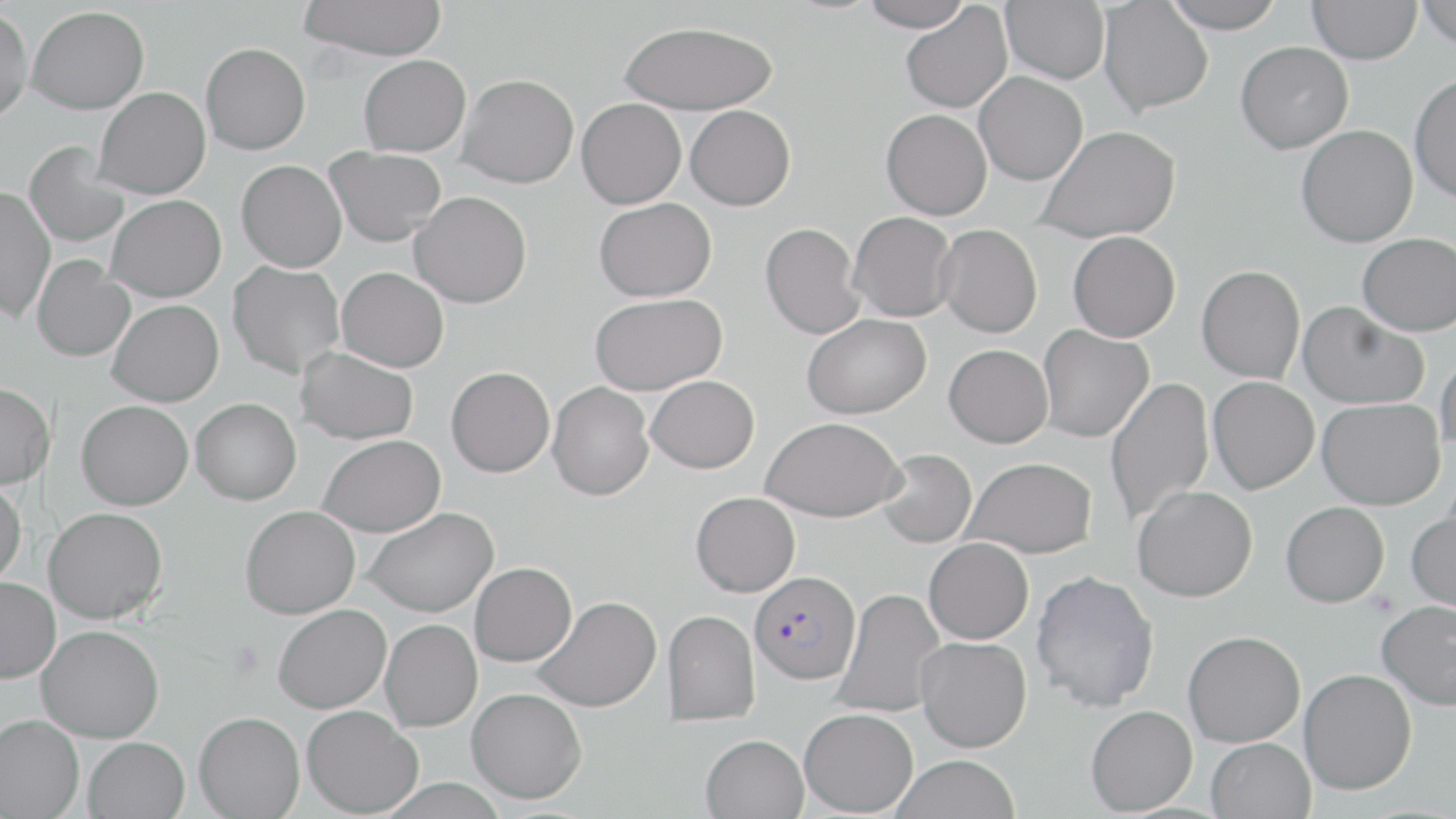
Summary:
  - Coordinate format: approximate bounding boxes as (x1,y1)-(x2,y2) corner pairs in pixels
  - Uninfected red blood cell locations: (297,0)-(448,60), (859,0)-(972,31), (1001,0)-(1109,84), (1160,0)-(1286,32), (1307,0)-(1421,64), (1417,0)-(1456,50), (1098,1)-(1213,116), (900,3)-(1012,114), (26,5)-(149,114), (0,6)-(34,123), (618,20)-(778,115), (1236,41)-(1353,154), (200,42)-(311,154), (359,54)-(471,155), (974,72)-(1087,186), (1410,72)-(1456,203), (458,74)-(579,188), (93,86)-(210,198), (576,97)-(686,208), (685,105)-(795,210), (881,108)-(992,220), (1035,125)-(1182,243), (1296,125)-(1418,247), (25,141)-(131,248), (324,146)-(446,246), (236,160)-(347,272), (0,186)-(55,322), (409,191)-(532,308), (106,194)-(226,301), (594,198)-(716,301), (848,211)-(957,322), (760,222)-(865,339), (936,223)-(1042,337), (1068,231)-(1181,342), (1357,232)-(1456,336), (31,255)-(135,362), (228,260)-(345,378), (1196,264)-(1305,383), (337,267)-(449,372), (590,293)-(727,395), (107,299)-(224,406), (1298,301)-(1429,409), (802,314)-(932,418), (1037,324)-(1153,442), (944,344)-(1053,447), (295,346)-(418,444), (1436,353)-(1456,458), (446,366)-(555,477), (646,375)-(759,473), (1105,376)-(1214,526), (1208,376)-(1320,493), (0,381)-(55,488), (547,382)-(654,500), (191,398)-(302,505), (1317,398)-(1445,509), (76,400)-(193,509), (761,417)-(905,521), (318,434)-(445,537), (876,448)-(976,548), (965,457)-(1097,557), (0,480)-(26,588), (1133,485)-(1258,602), (691,491)-(800,596), (1281,501)-(1389,607), (240,505)-(360,618), (43,506)-(168,624), (362,507)-(498,618), (1407,510)-(1456,614), (924,537)-(1034,644), (470,562)-(577,666), (1031,570)-(1160,711), (0,576)-(60,683), (833,587)-(948,719), (533,596)-(662,711), (1376,600)-(1456,710), (273,604)-(391,713), (662,609)-(760,725), (381,619)-(483,731), (37,624)-(164,742), (1183,630)-(1305,746), (915,636)-(1032,752), (1299,668)-(1417,794), (467,687)-(587,803), (301,705)-(423,817), (1085,705)-(1198,815), (799,708)-(918,816), (194,711)-(305,818), (0,714)-(84,818), (700,733)-(809,819), (83,736)-(190,819), (1206,737)-(1316,819), (890,754)-(1021,818)
  - Plasmodium falciparum-infected red blood cell locations: (749,570)-(860,685)
  - Slide-level diagnosis: Plasmodium falciparum
  - Modality: light microscopy
  - Magnification: 1000x
  - Field of view: single
  - Stain: May-Grünwald-Giemsa
  - Preparation: thin blood film
  - Image size: 1456×819 pixels